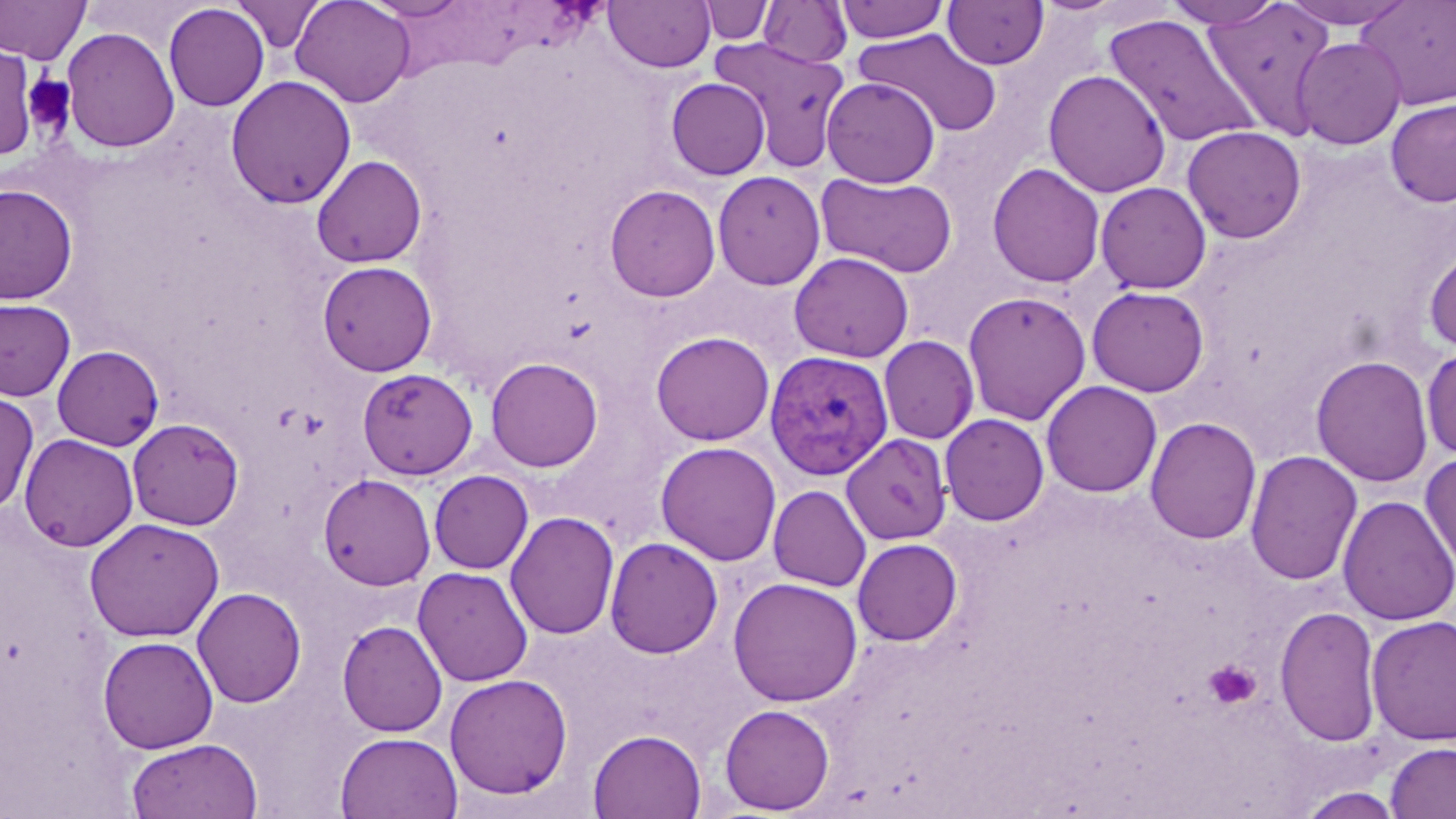

slide_level_diagnosis: Plasmodium vivax
platelet_locations: 'approximate bounding boxes as [x1, y1, x2, y2] in pixels: [22, 73, 76, 135], [1203, 660, 1261, 709]'
preparation: thin blood film
stain: May-Grünwald-Giemsa
image_size: 1456×819 pixels
plasmodium_vivax_infected_red_blood_cell_locations: 'approximate bounding boxes as [x1, y1, x2, y2] in pixels: [764, 350, 893, 480]'
magnification: 1000x
modality: optical microscopy
field_of_view: single
uninfected_red_blood_cell_locations: 'approximate bounding boxes as [x1, y1, x2, y2] in pixels: [0, 0, 91, 63], [232, 0, 326, 54], [290, 0, 415, 107], [360, 0, 473, 20], [604, 0, 716, 72], [835, 0, 949, 43], [942, 0, 1049, 69], [1163, 0, 1284, 29], [1277, 0, 1418, 29], [1356, 0, 1456, 110], [699, 1, 775, 45], [758, 1, 852, 68], [1202, 1, 1336, 137], [164, 3, 269, 111], [1104, 15, 1262, 149], [61, 26, 180, 152], [855, 27, 1002, 138], [709, 36, 849, 174], [1293, 36, 1407, 150], [0, 45, 37, 161], [1043, 70, 1171, 198], [225, 75, 357, 209], [821, 77, 940, 188], [666, 78, 770, 180], [1385, 98, 1456, 208], [1182, 125, 1306, 243], [311, 155, 427, 268], [987, 162, 1106, 288], [712, 171, 826, 290], [816, 172, 958, 278], [1095, 181, 1211, 294], [0, 184, 78, 305], [604, 184, 721, 302], [1424, 246, 1456, 355], [789, 251, 914, 363], [317, 261, 437, 376], [1086, 285, 1210, 397], [962, 290, 1091, 426], [0, 298, 75, 402], [650, 331, 774, 446], [878, 335, 979, 444], [52, 345, 164, 450], [1421, 346, 1456, 460], [1311, 355, 1433, 488], [486, 356, 603, 472], [357, 368, 478, 480], [1040, 380, 1163, 498], [0, 390, 39, 515], [939, 413, 1050, 526], [1144, 416, 1262, 545], [127, 418, 244, 530], [841, 433, 952, 544], [19, 434, 139, 551], [655, 441, 781, 565], [1245, 449, 1362, 586], [1420, 450, 1456, 579], [429, 470, 533, 574], [318, 473, 436, 590], [768, 484, 872, 591], [1337, 495, 1456, 626], [505, 511, 620, 641], [84, 518, 225, 642], [605, 536, 723, 659], [852, 537, 962, 645], [413, 565, 534, 686], [728, 577, 863, 707], [192, 587, 307, 708], [1275, 605, 1383, 748], [1366, 615, 1456, 746], [337, 620, 448, 737], [97, 636, 218, 754], [444, 674, 573, 800], [719, 704, 835, 815], [587, 728, 707, 818], [334, 731, 463, 819], [126, 738, 263, 818], [1385, 742, 1456, 819], [1296, 787, 1404, 819]'